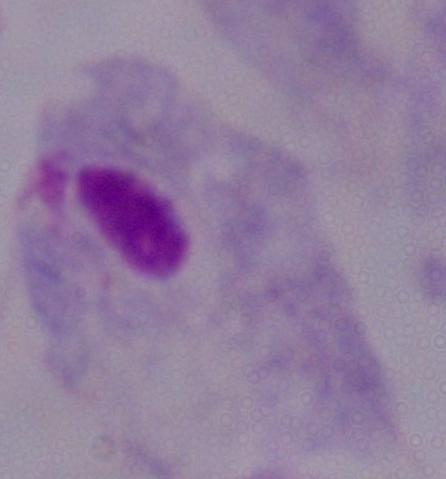

A trichomonad is shown. Micrograph. Captured at 1000x magnification.